Identify the parasite.
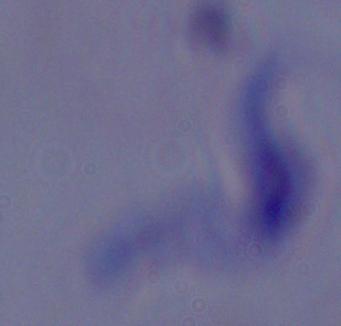
This is a trypanosome.

1000x magnification. Micrograph.